Locate and identify every blood parasite.
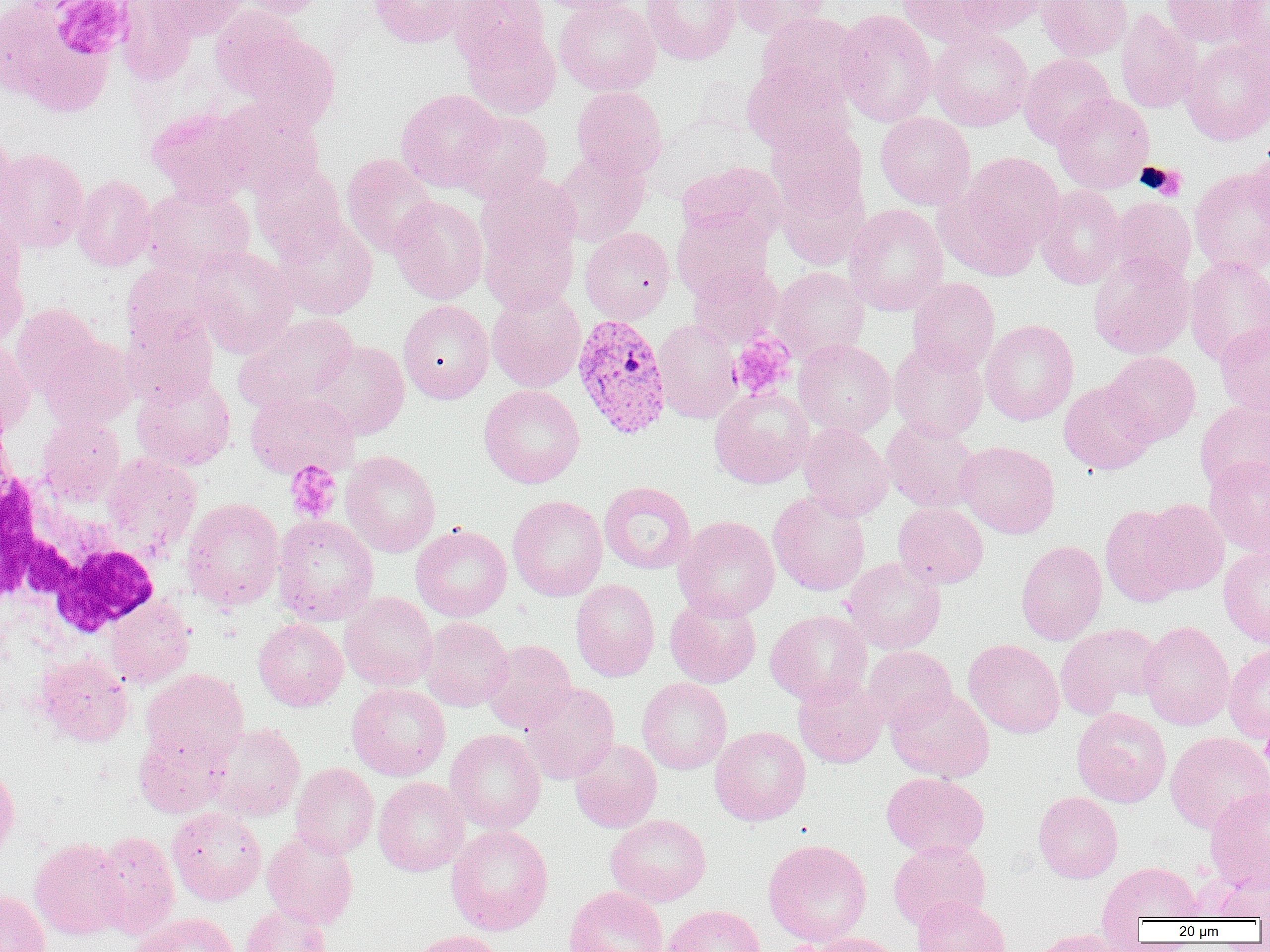

Approximate bounding boxes as [x1, y1, x2, y2] in pixels.
Plasmodium vivax-infected red blood cells: [572, 314, 672, 439].
No Plasmodium falciparum, Plasmodium ovale, Plasmodium malariae, Babesia divergens, or Trypanosoma brucei observed.

White blood cell locations: [1, 458, 161, 642]. Platelet locations: [54, 1, 131, 59], [1139, 163, 1188, 199], [729, 335, 795, 400], [285, 460, 342, 522], [1260, 721, 1270, 778], [776, 942, 830, 952]. Uninfected red blood cell locations: [115, 0, 197, 86], [147, 0, 249, 41], [237, 0, 330, 18], [369, 0, 467, 48], [450, 0, 549, 66], [533, 0, 638, 14], [554, 0, 660, 96], [642, 0, 739, 64], [728, 0, 830, 40], [898, 0, 1007, 48], [955, 0, 1049, 34], [1036, 0, 1133, 60], [1162, 0, 1264, 48], [0, 1, 117, 115], [1227, 1, 1270, 61], [210, 8, 305, 98], [835, 9, 938, 127], [1115, 9, 1202, 114], [757, 12, 865, 104], [462, 25, 561, 118], [927, 28, 1034, 131], [239, 32, 340, 132], [1181, 37, 1270, 145], [1019, 53, 1117, 148], [742, 63, 854, 156], [571, 86, 667, 180], [396, 88, 504, 192], [1052, 93, 1155, 193], [216, 98, 324, 195], [147, 106, 254, 204], [453, 111, 553, 202], [875, 112, 975, 210], [767, 122, 867, 217], [0, 128, 19, 226], [1249, 142, 1270, 229], [0, 147, 89, 253], [552, 150, 650, 246], [951, 151, 1065, 261], [341, 154, 439, 257], [250, 160, 348, 262], [678, 162, 787, 246], [1190, 166, 1270, 274], [775, 169, 871, 269], [476, 172, 580, 272], [72, 175, 156, 272], [141, 185, 255, 277], [1034, 185, 1128, 289], [389, 196, 488, 304], [1106, 196, 1196, 284], [844, 203, 948, 315], [672, 207, 773, 300], [0, 210, 25, 294], [478, 214, 579, 315], [272, 217, 378, 319], [580, 227, 675, 324], [191, 245, 298, 356], [1089, 252, 1194, 359], [1184, 256, 1270, 365], [122, 261, 215, 348], [689, 262, 782, 348], [0, 263, 27, 351], [771, 266, 870, 362], [906, 277, 1000, 374], [486, 288, 586, 393], [398, 300, 494, 404], [10, 303, 101, 397], [234, 312, 359, 412], [123, 313, 218, 406], [653, 319, 742, 423], [979, 319, 1079, 425], [1215, 321, 1270, 417], [40, 336, 138, 430], [794, 339, 896, 437], [307, 340, 410, 440], [889, 340, 988, 441], [0, 342, 35, 437], [1104, 351, 1201, 444], [132, 372, 236, 471], [1059, 380, 1158, 474], [479, 385, 584, 488], [710, 387, 814, 488], [245, 389, 359, 478], [1195, 401, 1270, 494], [37, 415, 125, 504], [882, 417, 982, 513], [798, 423, 894, 521], [957, 441, 1059, 538], [341, 451, 441, 557], [102, 452, 202, 554], [1204, 455, 1270, 555], [599, 481, 696, 574], [768, 491, 871, 596], [508, 495, 608, 601], [181, 497, 285, 611], [1139, 498, 1229, 596], [893, 502, 989, 588], [1100, 504, 1189, 606], [272, 515, 378, 625], [673, 515, 780, 621], [411, 524, 512, 621], [1016, 540, 1107, 645], [1219, 545, 1270, 647], [842, 557, 946, 653], [571, 579, 660, 681], [340, 591, 438, 691], [665, 593, 761, 688], [105, 596, 195, 687], [765, 609, 871, 706], [420, 617, 513, 711], [253, 618, 348, 711], [1138, 620, 1235, 730], [1056, 623, 1164, 717], [964, 639, 1065, 738], [481, 640, 577, 733], [1223, 644, 1270, 744], [862, 645, 957, 729], [35, 653, 132, 746], [141, 669, 249, 766], [793, 675, 886, 768], [637, 677, 732, 774], [520, 682, 619, 784], [347, 683, 451, 780], [886, 687, 994, 782], [1072, 707, 1171, 807], [209, 723, 305, 821], [710, 726, 811, 825], [445, 728, 546, 834], [1165, 732, 1270, 835], [134, 733, 227, 818], [569, 738, 662, 833], [290, 762, 379, 858], [0, 764, 20, 861], [881, 771, 989, 859], [373, 777, 470, 876], [1204, 787, 1270, 893], [1034, 791, 1123, 883], [167, 807, 267, 905], [606, 814, 711, 906], [446, 825, 553, 935], [262, 830, 359, 930], [94, 831, 180, 938], [29, 837, 130, 941], [763, 838, 872, 946], [889, 840, 990, 929], [1098, 861, 1204, 928], [1211, 873, 1270, 921], [563, 886, 669, 952], [0, 890, 50, 952], [912, 895, 1011, 952], [663, 904, 766, 952], [240, 905, 332, 952], [131, 913, 240, 952], [1027, 928, 1135, 952], [404, 930, 506, 952], [805, 932, 905, 952]. Slide-level diagnosis: Plasmodium vivax. One field of a larger specimen. Image is 1270×952 pixels. Thin blood film. Captured at 1000x magnification. Light microscopy.